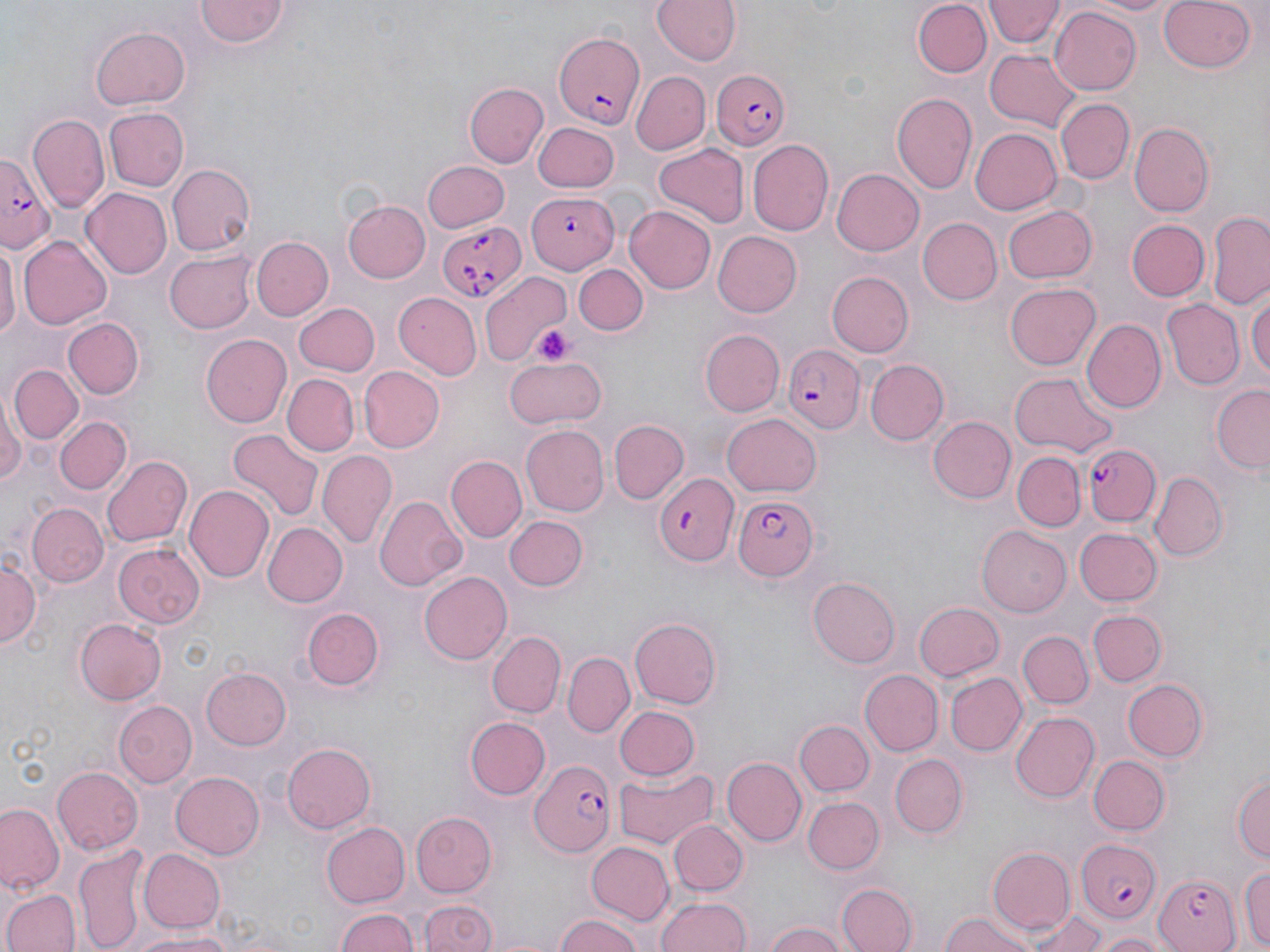
slide_level_diagnosis: Plasmodium falciparum
modality: light microscopy
image_size: 1270×952 pixels
field_of_view: single
magnification: 1000x
stain: May-Grünwald-Giemsa
preparation: thin blood smear
uninfected_red_blood_cell_locations: 'approximate bounding boxes as (x1, y1, x2, y2) in pixels: (650, 0, 745, 67), (987, 0, 1061, 49), (1085, 0, 1181, 17), (1159, 0, 1258, 73), (196, 1, 290, 49), (914, 2, 991, 78), (1050, 5, 1142, 95), (90, 27, 190, 111), (984, 46, 1083, 132), (630, 72, 710, 155), (463, 81, 549, 169), (891, 93, 976, 193), (1056, 98, 1133, 183), (104, 107, 189, 191), (28, 114, 110, 209), (534, 122, 620, 192), (1128, 123, 1214, 217), (969, 127, 1062, 216), (746, 140, 832, 237), (655, 144, 749, 227), (422, 161, 510, 233), (166, 164, 256, 257), (832, 168, 925, 255), (81, 189, 174, 278), (342, 198, 431, 283), (1003, 203, 1096, 283), (625, 205, 716, 294), (1207, 211, 1270, 308), (916, 217, 1003, 305), (1125, 219, 1210, 301), (712, 231, 803, 317), (18, 235, 113, 328), (250, 236, 334, 322), (1, 239, 18, 348), (165, 252, 257, 333), (573, 262, 648, 334), (825, 271, 913, 357), (480, 273, 574, 363), (1006, 282, 1101, 370), (392, 290, 481, 379), (1247, 293, 1270, 387), (1161, 298, 1244, 390), (294, 302, 380, 377), (61, 317, 144, 399), (1081, 319, 1164, 411), (700, 329, 783, 415), (200, 333, 291, 429), (505, 356, 608, 427), (867, 359, 947, 445), (8, 365, 80, 444), (358, 367, 444, 453), (1011, 370, 1117, 458), (284, 375, 358, 456), (1210, 384, 1270, 475), (0, 398, 24, 489), (722, 414, 820, 497), (52, 416, 131, 494), (930, 417, 1016, 504), (609, 420, 688, 503), (519, 425, 608, 517), (227, 429, 325, 523), (316, 451, 397, 549), (1013, 453, 1085, 532), (103, 454, 192, 547), (445, 455, 525, 543), (1150, 471, 1225, 560), (185, 485, 273, 585), (375, 496, 465, 589), (27, 503, 107, 585), (505, 514, 587, 590), (264, 521, 347, 608), (977, 525, 1069, 617), (1073, 527, 1161, 606), (114, 543, 205, 630), (0, 557, 41, 648), (418, 570, 512, 665), (808, 578, 900, 667), (914, 603, 1005, 681), (302, 605, 383, 688), (1089, 609, 1166, 687), (72, 616, 166, 705), (628, 618, 720, 709), (1017, 630, 1093, 709), (489, 631, 565, 718), (565, 653, 633, 740), (200, 667, 292, 751), (858, 670, 942, 756), (947, 671, 1024, 755), (1123, 677, 1209, 761), (112, 700, 196, 788), (613, 705, 700, 782), (1009, 711, 1099, 803), (464, 716, 549, 799), (795, 719, 873, 796), (281, 743, 374, 834), (891, 753, 968, 838), (1089, 754, 1171, 834), (724, 756, 805, 845), (53, 766, 143, 855), (613, 767, 719, 851), (170, 772, 265, 860), (1232, 774, 1269, 867), (804, 796, 883, 873), (1, 804, 62, 891), (409, 812, 495, 897), (668, 819, 747, 896), (324, 821, 410, 908), (584, 843, 673, 924), (73, 845, 150, 952), (987, 846, 1075, 930), (138, 849, 225, 933), (1239, 864, 1270, 950), (839, 883, 917, 952), (2, 889, 77, 952), (960, 890, 1071, 952), (658, 895, 753, 952), (421, 899, 496, 952), (1021, 906, 1107, 951), (334, 907, 418, 952), (939, 910, 1041, 952), (552, 913, 646, 952), (765, 923, 847, 952), (128, 928, 240, 951), (1094, 929, 1172, 951)'
plasmodium_falciparum_infected_red_blood_cell_locations: 'approximate bounding boxes as (x1, y1, x2, y2) in pixels: (553, 29, 644, 126), (713, 69, 793, 152), (0, 147, 52, 246), (529, 194, 619, 271), (437, 222, 526, 303), (782, 344, 864, 431), (1079, 443, 1161, 528), (653, 472, 739, 566), (733, 494, 816, 582), (533, 760, 615, 853), (1074, 839, 1163, 922), (1151, 874, 1242, 952)'
platelet_locations: 'approximate bounding boxes as (x1, y1, x2, y2) in pixels: (535, 326, 572, 367)'